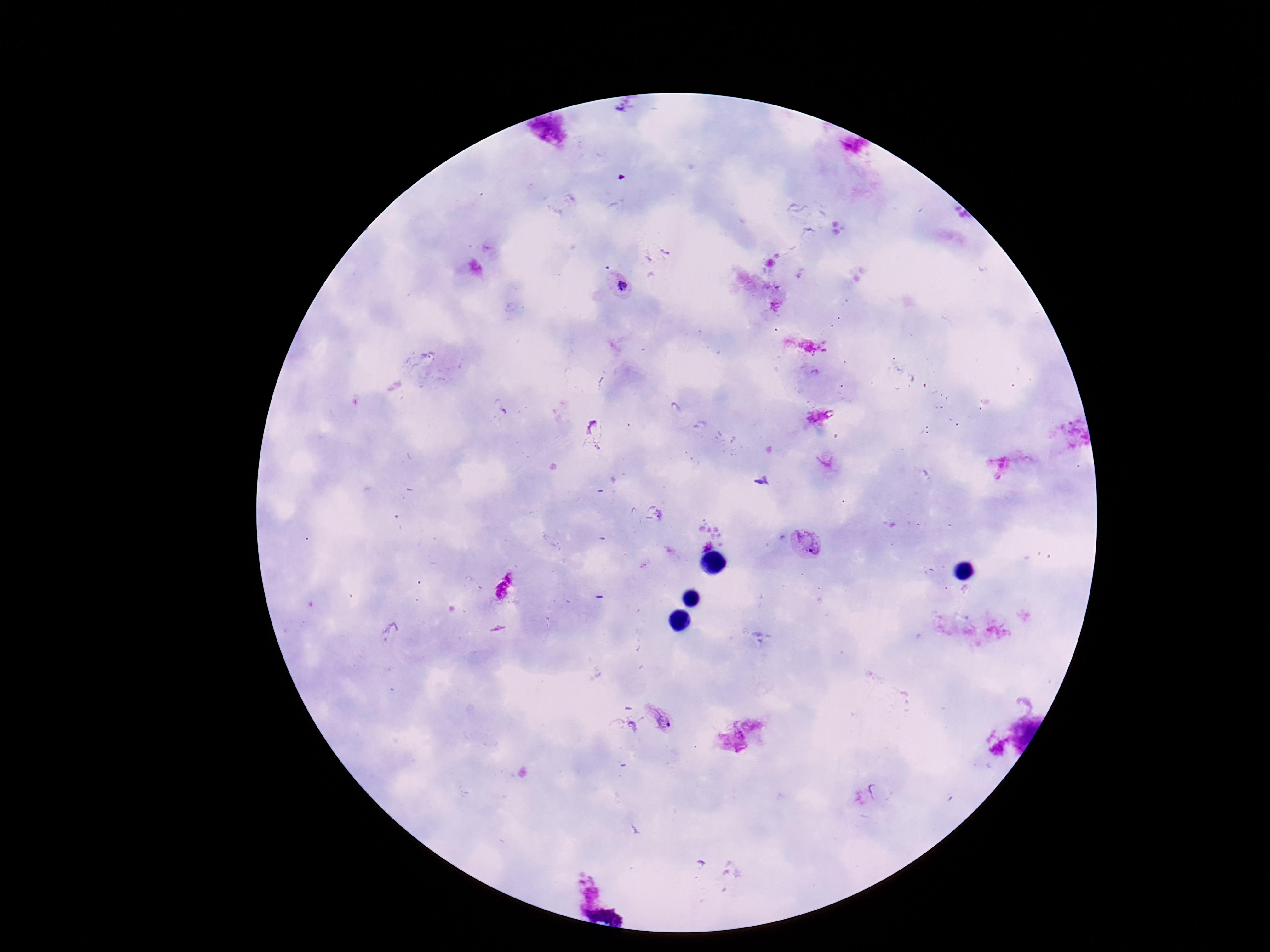 Approximate centers as [x, y] in pixels. Plasmodium parasite locations: [621, 288], [593, 430], [808, 545], [661, 719]. Giemsa-stained preparation. 100x magnification. Patient malaria status: positive. Image is 1270×952 pixels. One field from this slide. Photographed through the microscope eyepiece with a smartphone camera. Thick blood film.